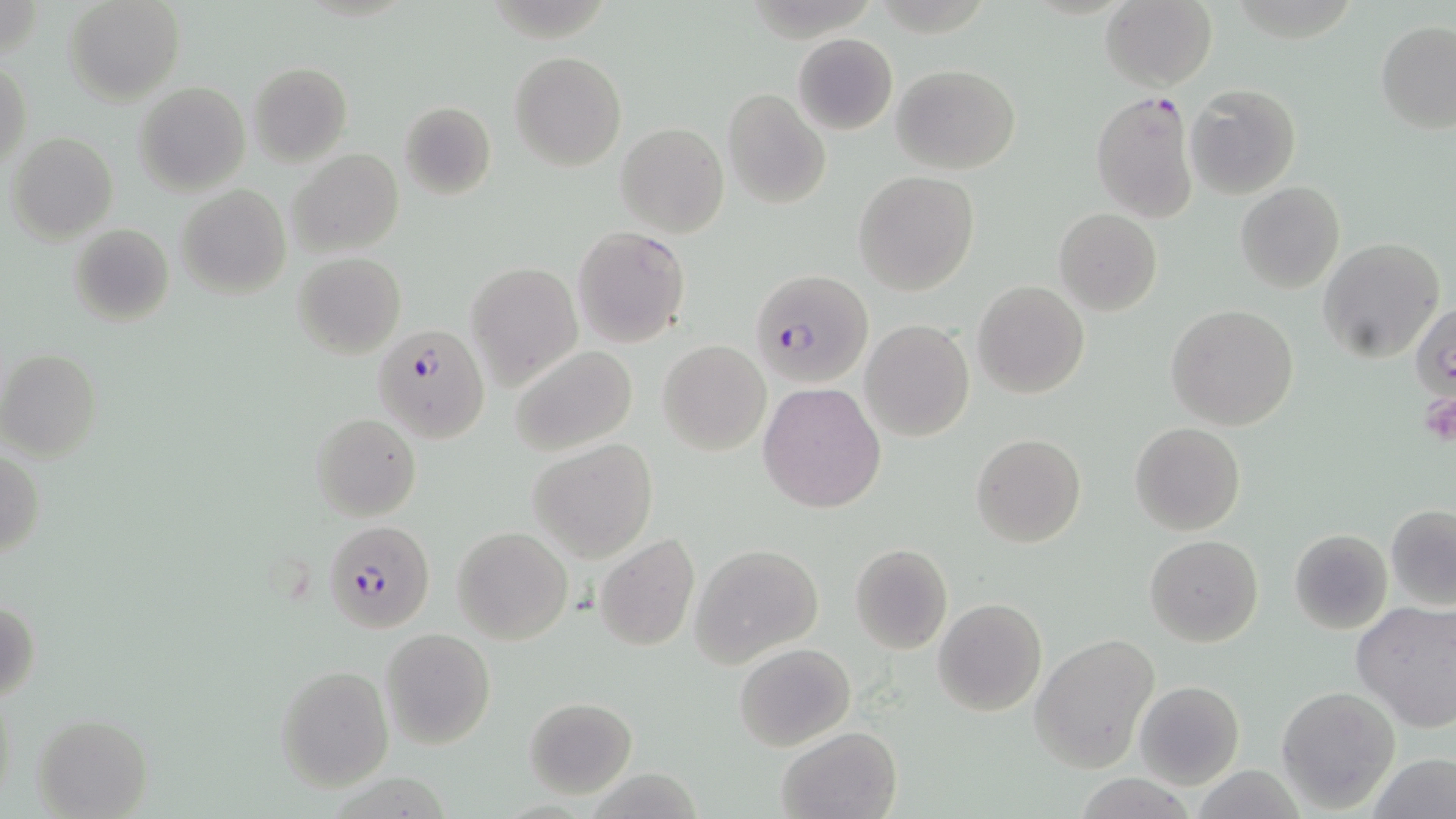
slide_level_diagnosis: Plasmodium falciparum
field_of_view: one of a larger specimen
uninfected_red_blood_cell_locations: 'approximate bounding boxes as (x1, y1, x2, y2) in pixels: (64, 0, 184, 104), (1101, 0, 1217, 91), (1375, 21, 1456, 134), (792, 32, 898, 136), (509, 51, 627, 171), (1, 57, 30, 169), (248, 63, 351, 165), (893, 64, 1021, 174), (135, 83, 250, 196), (1186, 83, 1302, 200), (723, 88, 830, 209), (399, 101, 497, 200), (616, 122, 729, 238), (7, 132, 118, 243), (289, 147, 402, 258), (853, 171, 979, 295), (1234, 182, 1345, 294), (175, 184, 290, 300), (1054, 210, 1161, 315), (69, 222, 175, 328), (572, 226, 690, 347), (1318, 236, 1447, 361), (292, 252, 406, 359), (466, 261, 583, 391), (972, 281, 1090, 400), (1410, 303, 1456, 397), (1165, 304, 1300, 431), (861, 320, 973, 440), (658, 340, 771, 456), (508, 345, 638, 455), (0, 349, 101, 462), (758, 381, 886, 513), (311, 412, 422, 521), (1131, 421, 1245, 536), (971, 433, 1085, 547), (528, 439, 658, 563), (1, 451, 44, 560), (1385, 505, 1456, 609), (452, 527, 574, 646), (1288, 529, 1392, 633), (594, 533, 701, 654), (1145, 535, 1263, 647), (689, 543, 823, 665), (849, 543, 953, 654), (934, 598, 1047, 716), (1, 599, 42, 705), (1352, 601, 1456, 732), (381, 627, 495, 750), (1031, 634, 1158, 771), (734, 642, 856, 751), (276, 664, 394, 791), (1133, 679, 1244, 789), (1277, 687, 1400, 811), (522, 697, 637, 799), (34, 714, 153, 818), (776, 727, 902, 819), (1372, 754, 1456, 819)'
preparation: thin blood film
modality: optical microscopy
plasmodium_falciparum_infected_red_blood_cell_locations: 'approximate bounding boxes as (x1, y1, x2, y2) in pixels: (1089, 92, 1198, 222), (751, 270, 874, 389), (370, 327, 490, 447), (323, 519, 435, 634)'
image_size: 1456×819 pixels
magnification: 1000x
platelet_locations: 'approximate bounding boxes as (x1, y1, x2, y2) in pixels: (1417, 391, 1456, 448)'
stain: May-Grünwald-Giemsa